Mark where platelets are.
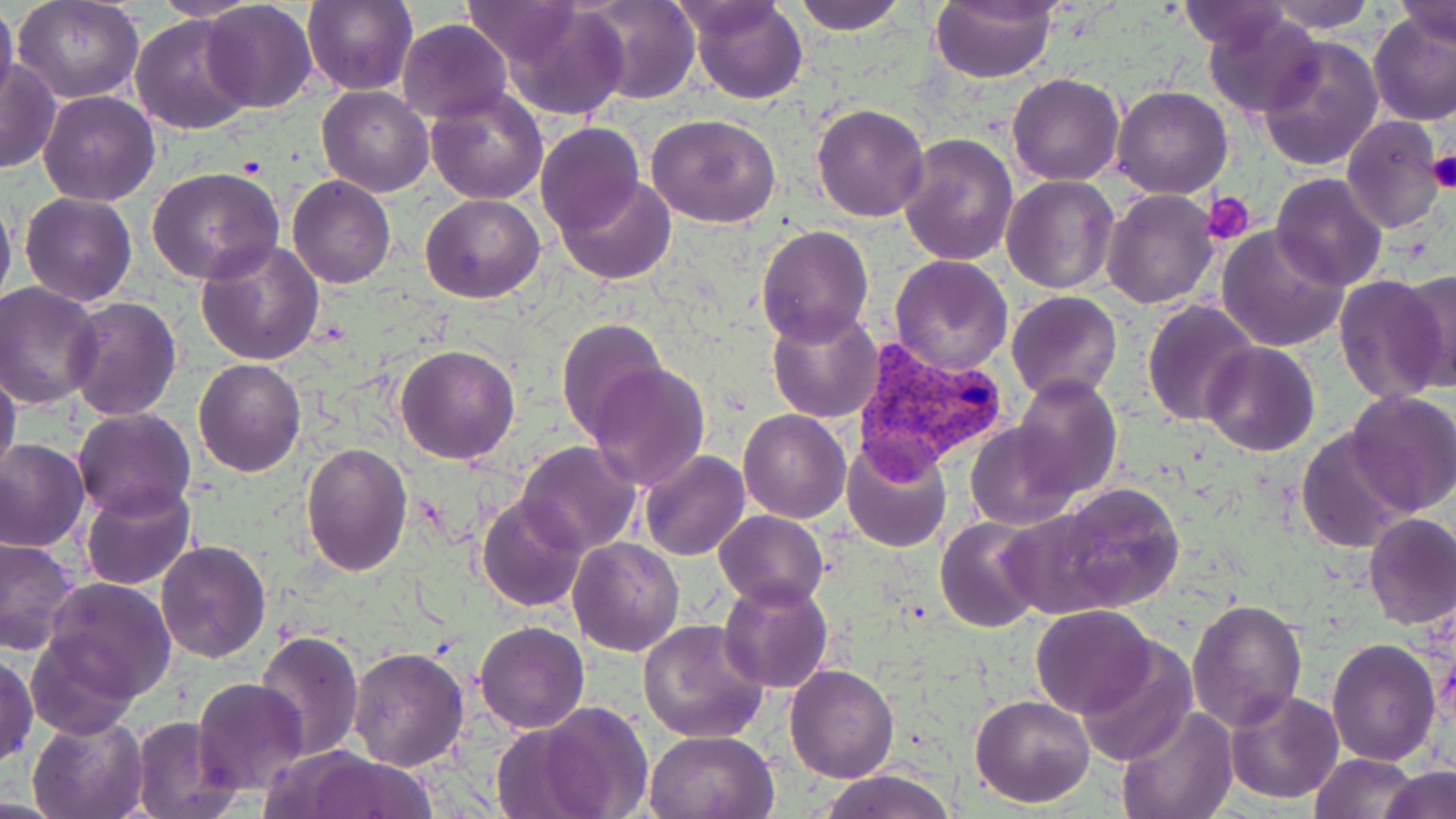

Approximate bounding boxes as (x1,y1)-(x2,y2) corner pairs in pixels.
Platelets: (1427,148)-(1456,195), (1206,194)-(1255,242).

slide-level diagnosis = Plasmodium vivax
magnification = 1000x
Plasmodium vivax-infected red blood cell locations = approximate bounding boxes as (x1,y1)-(x2,y2) corner pairs in pixels: (856,344)-(1005,488)
uninfected red blood cell locations = approximate bounding boxes as (x1,y1)-(x2,y2) corner pairs in pixels: (15,0)-(143,103), (149,0)-(258,21), (579,0)-(702,105), (687,0)-(807,104), (788,0)-(907,35), (929,0)-(1057,84), (1263,0)-(1378,32), (1398,0)-(1456,48), (201,1)-(317,114), (302,1)-(419,95), (1178,1)-(1289,51), (0,2)-(18,108), (463,2)-(589,66), (490,2)-(633,122), (1205,9)-(1322,118), (1368,11)-(1456,126), (130,15)-(256,136), (396,20)-(513,123), (1257,34)-(1383,171), (0,59)-(60,174), (1006,73)-(1124,186), (316,86)-(435,196), (426,86)-(547,204), (1113,86)-(1233,199), (39,90)-(160,205), (811,102)-(930,222), (646,113)-(781,227), (1341,115)-(1445,235), (535,122)-(645,237), (898,133)-(1019,265), (147,167)-(284,284), (1270,173)-(1389,290), (555,174)-(677,285), (1002,174)-(1119,294), (287,176)-(397,290), (0,189)-(16,320), (1101,191)-(1219,310), (20,193)-(137,306), (420,194)-(546,304), (756,225)-(874,347), (1218,225)-(1348,352), (194,237)-(326,368), (890,255)-(1015,374), (1397,267)-(1456,393), (1333,274)-(1450,405), (1,284)-(105,408), (1007,290)-(1121,404), (63,298)-(181,420), (1142,298)-(1259,426), (767,305)-(883,422), (555,318)-(667,439), (1202,342)-(1319,456), (395,345)-(521,465), (194,358)-(305,476), (586,361)-(711,489), (0,365)-(22,488), (1014,374)-(1123,500), (1344,389)-(1456,516), (72,407)-(196,522), (739,410)-(851,523), (966,422)-(1080,527), (1296,427)-(1413,554), (0,438)-(89,552), (840,438)-(953,555), (516,441)-(642,556), (300,442)-(412,576), (639,450)-(750,562), (81,482)-(194,589), (1037,482)-(1187,616), (477,494)-(588,613), (714,509)-(828,610), (1363,512)-(1456,630), (935,515)-(1046,632), (0,538)-(79,658), (569,538)-(686,656), (155,539)-(271,663), (43,577)-(176,703), (717,577)-(833,695), (1187,599)-(1306,731), (1030,604)-(1156,718), (638,619)-(769,742), (474,621)-(590,734), (255,629)-(366,761), (27,632)-(139,739), (1073,638)-(1197,765), (1326,638)-(1441,767), (348,646)-(469,769), (1,655)-(37,766), (785,665)-(897,782), (192,677)-(309,794), (1224,690)-(1342,806), (970,693)-(1095,807), (521,700)-(653,819), (1116,704)-(1237,819), (28,713)-(147,819), (129,715)-(242,818), (644,729)-(778,818), (298,751)-(436,819), (1311,753)-(1419,819), (1378,766)-(1456,819), (820,769)-(955,819)
preparation = thin blood smear
stain = May-Grünwald-Giemsa
field of view = one of a larger specimen
modality = optical microscopy
image size = 1456×819 pixels